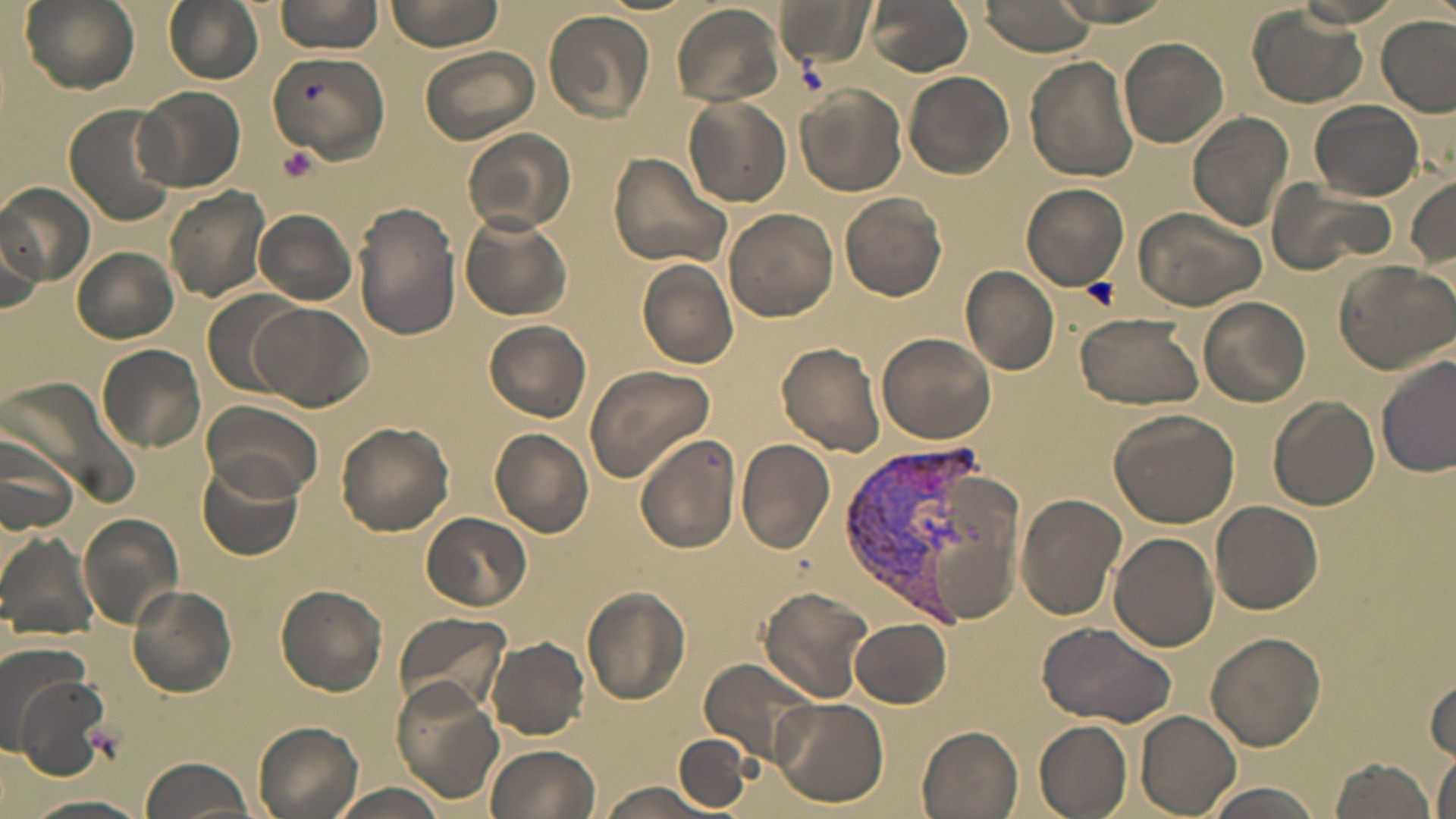 Approximate bounding boxes as named x1/y1/x2/y2 corners in pixels. Uninfected red blood cell locations: (x1=19, y1=0, x2=138, y2=94), (x1=274, y1=0, x2=382, y2=55), (x1=383, y1=0, x2=508, y2=52), (x1=774, y1=0, x2=875, y2=69), (x1=864, y1=0, x2=974, y2=75), (x1=973, y1=0, x2=1097, y2=55), (x1=162, y1=1, x2=262, y2=84), (x1=670, y1=3, x2=786, y2=107), (x1=1248, y1=6, x2=1367, y2=108), (x1=544, y1=9, x2=655, y2=124), (x1=1376, y1=16, x2=1456, y2=115), (x1=1118, y1=37, x2=1229, y2=147), (x1=419, y1=48, x2=539, y2=144), (x1=266, y1=50, x2=390, y2=165), (x1=1026, y1=56, x2=1139, y2=182), (x1=903, y1=72, x2=1012, y2=179), (x1=135, y1=85, x2=246, y2=193), (x1=797, y1=87, x2=906, y2=194), (x1=683, y1=95, x2=792, y2=207), (x1=1310, y1=101, x2=1424, y2=201), (x1=65, y1=105, x2=178, y2=226), (x1=1187, y1=110, x2=1295, y2=230), (x1=464, y1=128, x2=576, y2=234), (x1=607, y1=152, x2=733, y2=268), (x1=1407, y1=177, x2=1456, y2=268), (x1=1267, y1=181, x2=1396, y2=276), (x1=1022, y1=183, x2=1130, y2=291), (x1=0, y1=184, x2=94, y2=287), (x1=163, y1=187, x2=272, y2=301), (x1=840, y1=192, x2=947, y2=300), (x1=353, y1=203, x2=461, y2=341), (x1=1132, y1=205, x2=1266, y2=310), (x1=253, y1=209, x2=356, y2=305), (x1=723, y1=209, x2=838, y2=323), (x1=461, y1=212, x2=573, y2=321), (x1=0, y1=223, x2=44, y2=321), (x1=71, y1=247, x2=179, y2=343), (x1=637, y1=258, x2=738, y2=367), (x1=1332, y1=259, x2=1456, y2=373), (x1=961, y1=266, x2=1060, y2=376), (x1=201, y1=290, x2=303, y2=400), (x1=1198, y1=294, x2=1311, y2=407), (x1=251, y1=302, x2=373, y2=412), (x1=1075, y1=312, x2=1204, y2=409), (x1=483, y1=320, x2=592, y2=421), (x1=878, y1=330, x2=997, y2=443), (x1=777, y1=341, x2=885, y2=457), (x1=98, y1=344, x2=206, y2=452), (x1=1377, y1=355, x2=1456, y2=480), (x1=584, y1=365, x2=715, y2=481), (x1=1268, y1=396, x2=1378, y2=511), (x1=201, y1=400, x2=323, y2=504), (x1=1109, y1=409, x2=1240, y2=528), (x1=336, y1=421, x2=455, y2=536), (x1=490, y1=428, x2=593, y2=537), (x1=0, y1=434, x2=77, y2=536), (x1=635, y1=434, x2=741, y2=553), (x1=738, y1=438, x2=836, y2=553), (x1=196, y1=459, x2=302, y2=562), (x1=1017, y1=493, x2=1125, y2=620), (x1=1211, y1=500, x2=1323, y2=616), (x1=80, y1=512, x2=185, y2=627), (x1=421, y1=512, x2=531, y2=612), (x1=100, y1=528, x2=217, y2=670), (x1=0, y1=531, x2=98, y2=647), (x1=1109, y1=531, x2=1220, y2=653), (x1=128, y1=584, x2=238, y2=695), (x1=276, y1=584, x2=388, y2=694), (x1=758, y1=588, x2=873, y2=702), (x1=583, y1=589, x2=690, y2=703), (x1=392, y1=612, x2=511, y2=716), (x1=850, y1=617, x2=952, y2=707), (x1=1036, y1=622, x2=1173, y2=727), (x1=1207, y1=631, x2=1325, y2=751), (x1=487, y1=637, x2=589, y2=739), (x1=0, y1=638, x2=90, y2=741), (x1=700, y1=656, x2=820, y2=768), (x1=1427, y1=668, x2=1456, y2=763), (x1=12, y1=671, x2=118, y2=779), (x1=391, y1=683, x2=503, y2=801), (x1=770, y1=697, x2=889, y2=807), (x1=1135, y1=710, x2=1242, y2=818), (x1=1034, y1=720, x2=1133, y2=817), (x1=253, y1=722, x2=365, y2=819), (x1=918, y1=726, x2=1024, y2=819), (x1=674, y1=733, x2=753, y2=811), (x1=484, y1=743, x2=602, y2=819), (x1=1432, y1=749, x2=1455, y2=819), (x1=1327, y1=756, x2=1437, y2=819), (x1=138, y1=757, x2=255, y2=819), (x1=596, y1=782, x2=722, y2=819), (x1=332, y1=783, x2=442, y2=819), (x1=1200, y1=783, x2=1326, y2=819), (x1=21, y1=792, x2=153, y2=818). Plasmodium vivax-infected red blood cell locations: (x1=840, y1=434, x2=983, y2=620). Platelet locations: (x1=300, y1=79, x2=325, y2=105), (x1=279, y1=145, x2=319, y2=182), (x1=1083, y1=278, x2=1120, y2=308). Slide-level diagnosis: Plasmodium vivax. Captured at 1000x magnification. May-Grünwald-Giemsa-stained preparation. Image is 1456×819 pixels. Thin blood film. Single field of view. Light microscopy.